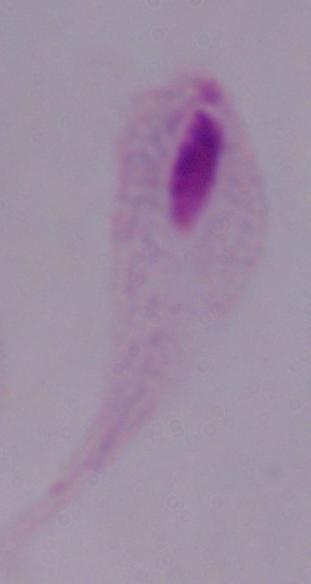

modality = micrograph
magnification = 1000x
identification = trichomonad